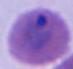

identification = Plasmodium
modality = photomicrograph
magnification = 400x or 1000x